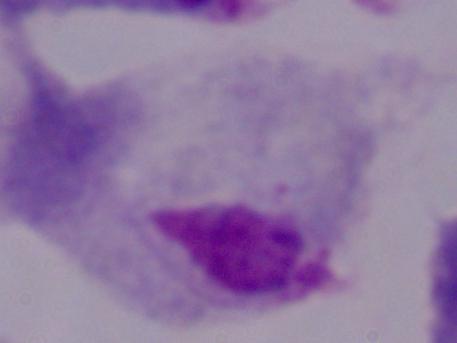

Summary:
  - Modality: photomicrograph
  - Magnification: 1000x
  - Identification: trichomonad